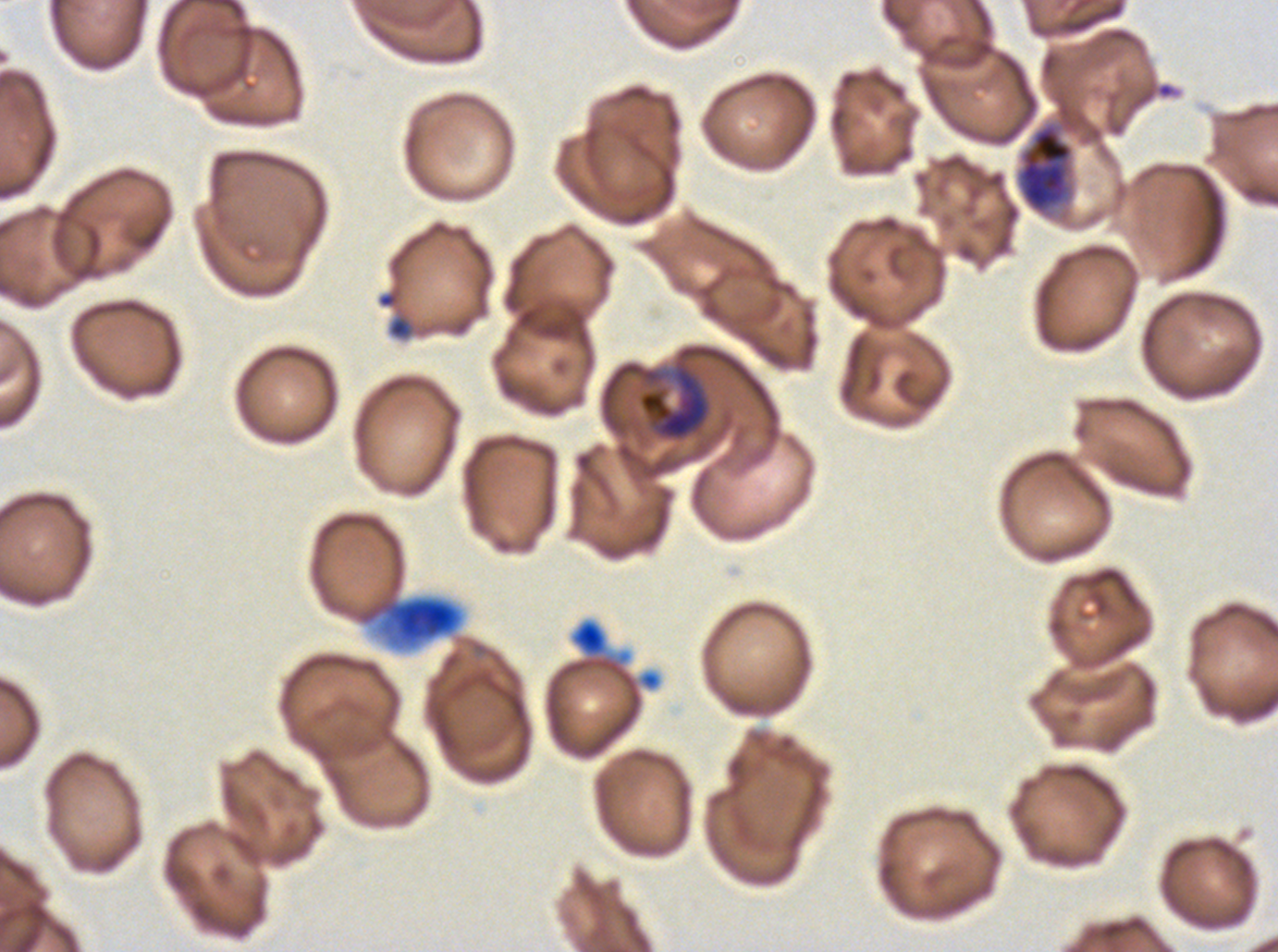 Approximate bounding boxes as {x1, y1, x2, y2} in pixels. Early schizont locations: {1015, 121, 1075, 216}. Late trophozoite locations: {637, 361, 711, 442}. Debris locations: {388, 316, 412, 339}, {392, 599, 457, 641}, {577, 623, 604, 652}. Life-cycle stages observed: late trophozoite, early schizont. P. falciparum cultured ex vivo for 24 to 48 hours, from a patient in The Gambia. Giemsa-stained preparation. Thin blood film. Image is 1278×952 pixels. A sub-image separated from a larger composite.